Name the parasite shown.
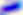

Toxoplasma gondii.

magnification = 400x
modality = micrograph